Identify the blood parasite species.
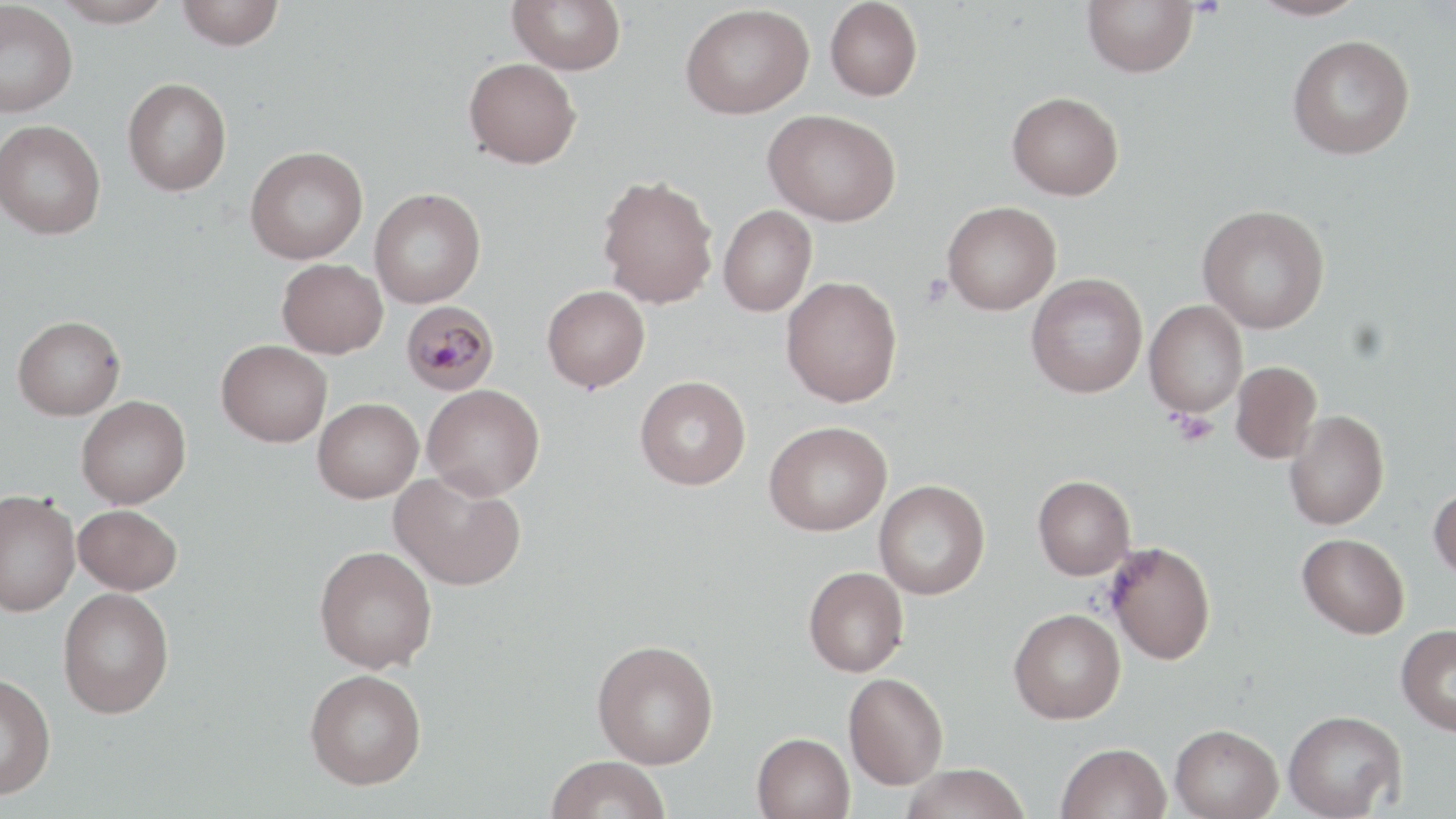

Plasmodium malariae.

stain: May-Grünwald-Giemsa
image_size: 1456×819 pixels
preparation: thin blood smear
uninfected_red_blood_cell_locations: 'approximate bounding boxes as (x1,y1)-(x2,y2) corner pairs in pixels: (52,0)-(173,28), (177,0)-(284,50), (507,0)-(626,75), (825,0)-(922,101), (1082,0)-(1200,77), (1249,0)-(1368,21), (0,2)-(78,116), (680,3)-(814,118), (1288,34)-(1415,159), (463,57)-(581,168), (122,78)-(232,196), (1007,91)-(1124,200), (764,108)-(901,226), (0,119)-(106,239), (245,145)-(368,264), (596,175)-(718,308), (369,188)-(486,308), (942,201)-(1061,315), (718,205)-(817,316), (1197,205)-(1330,333), (277,258)-(387,358), (1026,273)-(1147,398), (782,277)-(902,407), (542,284)-(650,392), (1144,300)-(1248,418), (12,315)-(125,419), (216,339)-(332,447), (1230,362)-(1321,464), (634,375)-(751,490), (422,384)-(545,500), (76,395)-(191,508), (313,398)-(423,503), (1284,410)-(1389,530), (764,421)-(892,535), (390,470)-(526,590), (1032,475)-(1135,580), (874,480)-(990,600), (1428,484)-(1456,584), (0,490)-(80,616), (73,504)-(182,595), (1298,533)-(1410,639), (1106,540)-(1216,665), (314,545)-(437,673), (804,566)-(909,676), (58,587)-(174,718), (1009,608)-(1126,724), (1396,624)-(1456,736), (592,639)-(719,768), (305,669)-(426,789), (0,673)-(56,798), (844,673)-(948,790), (1283,710)-(1407,818), (1170,723)-(1283,819), (752,732)-(855,819), (1057,742)-(1171,819), (545,755)-(671,819), (901,763)-(1032,819)'
magnification: 1000x
modality: optical microscopy
field_of_view: single
plasmodium_malariae_infected_red_blood_cell_locations: 'approximate bounding boxes as (x1,y1)-(x2,y2) corner pairs in pixels: (401,301)-(499,396)'
platelet_locations: 'approximate bounding boxes as (x1,y1)-(x2,y2) corner pairs in pixels: (920,275)-(954,307), (1171,411)-(1218,447)'